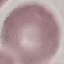
Result: no malaria parasites seen. Cell patch, automatically extracted from a larger field of view and resized to 64 × 64 pixels. Thin blood smear. Giemsa stain. Acquired by smartphone through the microscope eyepiece.